Identify the parasite.
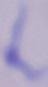

This is a trypanosome.

magnification = 1000x
modality = photomicrograph